Locate every leukocyte (white blood cell).
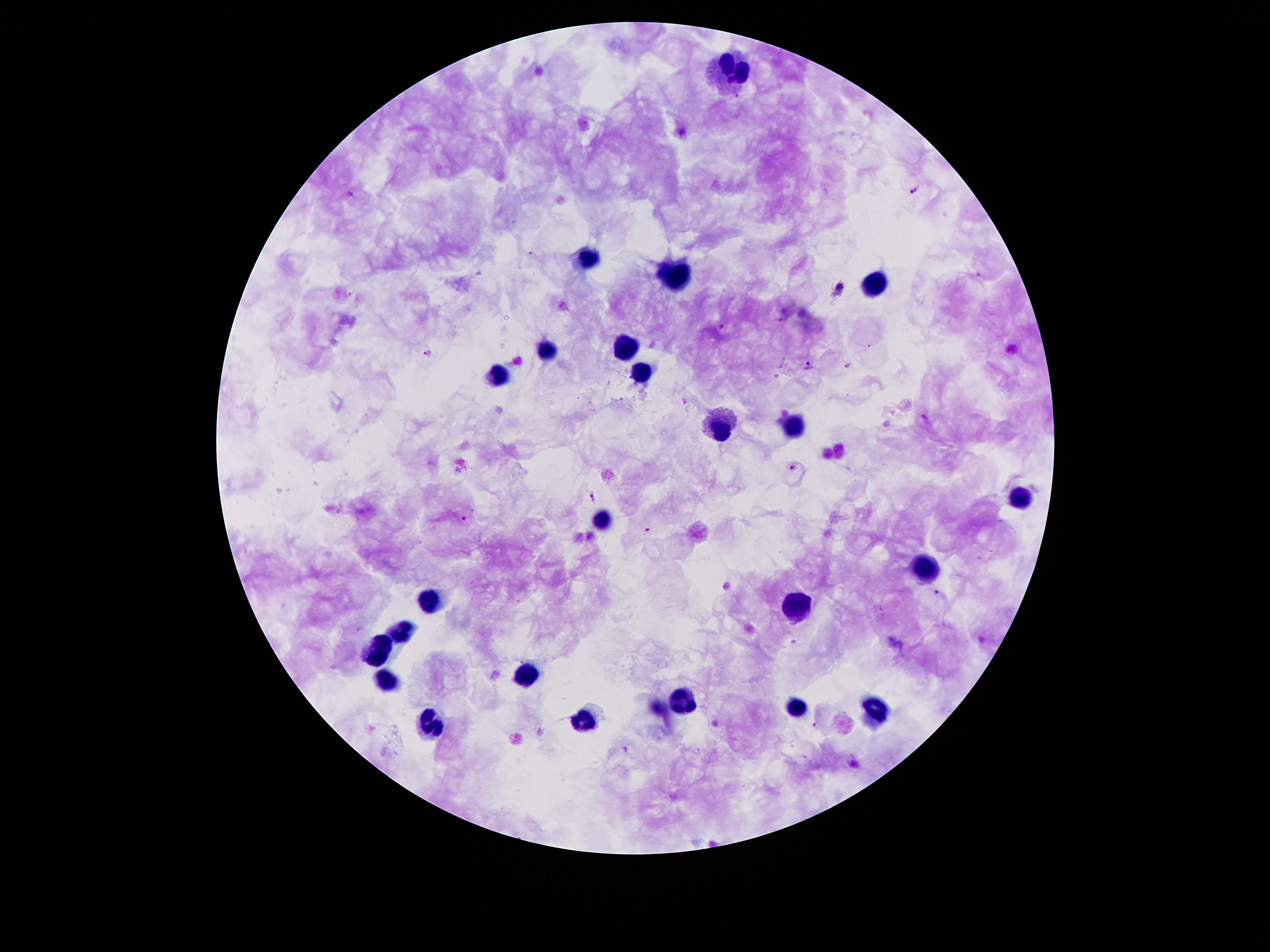
Approximate centers as (x, y) in pixels.
Leukocytes: (731, 76), (587, 256), (676, 275), (874, 285), (625, 346), (546, 350), (642, 373), (497, 377), (719, 427), (793, 427), (1021, 498), (602, 519), (925, 567), (429, 602), (797, 610), (401, 633), (380, 650), (528, 674), (390, 681), (683, 703), (798, 708), (877, 712), (582, 720), (429, 725).

malaria parasite locations = (915, 191), (840, 288), (722, 327), (428, 354), (808, 363), (846, 365), (792, 469), (592, 497), (462, 518), (648, 530), (937, 592), (816, 724)
preparation = thick peripheral-blood smear
patient malaria status = infected with Plasmodium falciparum
image size = 1270×952 pixels
stain = Giemsa
field of view = single
magnification = 100x
capture = smartphone through the microscope eyepiece